Describe the morphology of the erythrocytes.
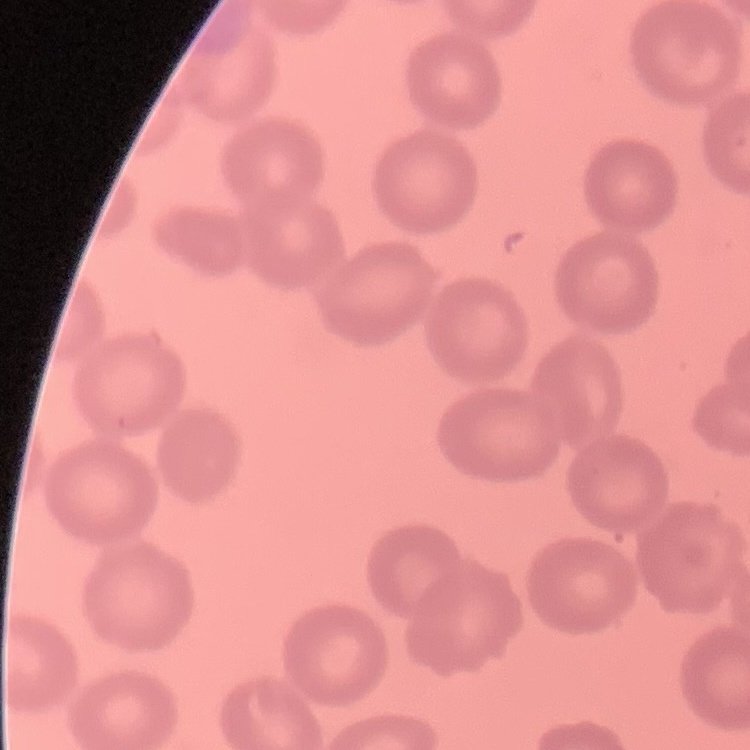
They show no rouleaux formation.

stain = Field's or Giemsa
preparation = thin blood film
image type = one tile cut from a larger photomicrograph